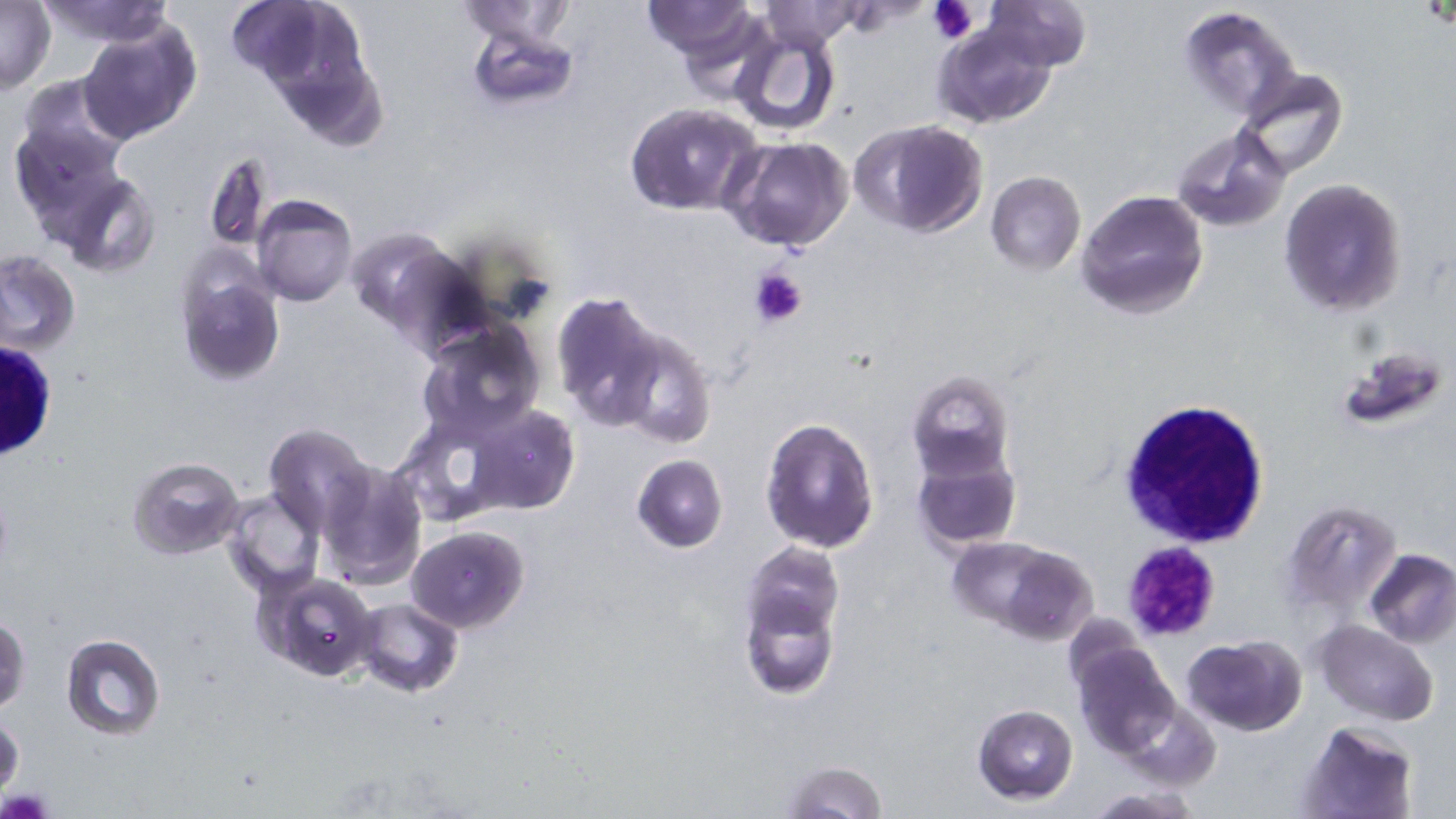

Approximate bounding boxes as [x1, y1, x2, y2] in pixels. Platelet locations: [927, 0, 980, 46], [749, 267, 807, 328], [1120, 541, 1223, 642]. Uninfected red blood cell locations: [37, 0, 177, 46], [249, 0, 389, 146], [980, 0, 1090, 70], [224, 1, 342, 95], [638, 1, 764, 61], [0, 2, 56, 94], [455, 3, 581, 50], [759, 3, 863, 50], [1177, 3, 1302, 119], [77, 17, 202, 147], [931, 17, 1059, 129], [464, 19, 580, 111], [726, 21, 842, 137], [1234, 68, 1348, 180], [624, 103, 764, 216], [9, 116, 131, 236], [852, 120, 987, 238], [1174, 127, 1287, 231], [722, 136, 855, 253], [203, 151, 276, 253], [54, 170, 160, 277], [984, 172, 1086, 275], [1278, 178, 1408, 319], [1076, 190, 1208, 320], [251, 195, 357, 307], [345, 225, 466, 340], [0, 250, 79, 354], [173, 252, 287, 388], [551, 296, 666, 435], [415, 319, 546, 443], [608, 324, 715, 450], [1334, 345, 1451, 434], [907, 371, 1015, 481], [464, 403, 579, 516], [761, 417, 879, 552], [264, 424, 373, 534], [912, 439, 1021, 551], [632, 454, 727, 553], [127, 455, 246, 561], [316, 461, 427, 592], [222, 490, 324, 596], [1280, 499, 1403, 616], [405, 525, 528, 633], [948, 537, 1096, 643], [741, 548, 844, 697], [1365, 549, 1456, 648], [254, 570, 382, 682], [354, 598, 464, 697], [1, 613, 30, 717], [1312, 620, 1439, 725], [60, 633, 166, 740], [1070, 635, 1181, 761], [1183, 635, 1306, 736], [1118, 701, 1222, 790], [972, 703, 1078, 802], [0, 712, 23, 796], [1298, 722, 1418, 818], [782, 760, 887, 818], [1082, 787, 1204, 817]. White blood cell locations: [1, 341, 58, 464], [1118, 398, 1269, 551]. Slide-level diagnosis: Plasmodium falciparum. Optical microscopy. Image is 1456×819 pixels. One field of a larger specimen. Captured at 1000x magnification. Thin blood smear. May-Grünwald-Giemsa-stained preparation.